Give the extent of all uninfected red blood cells.
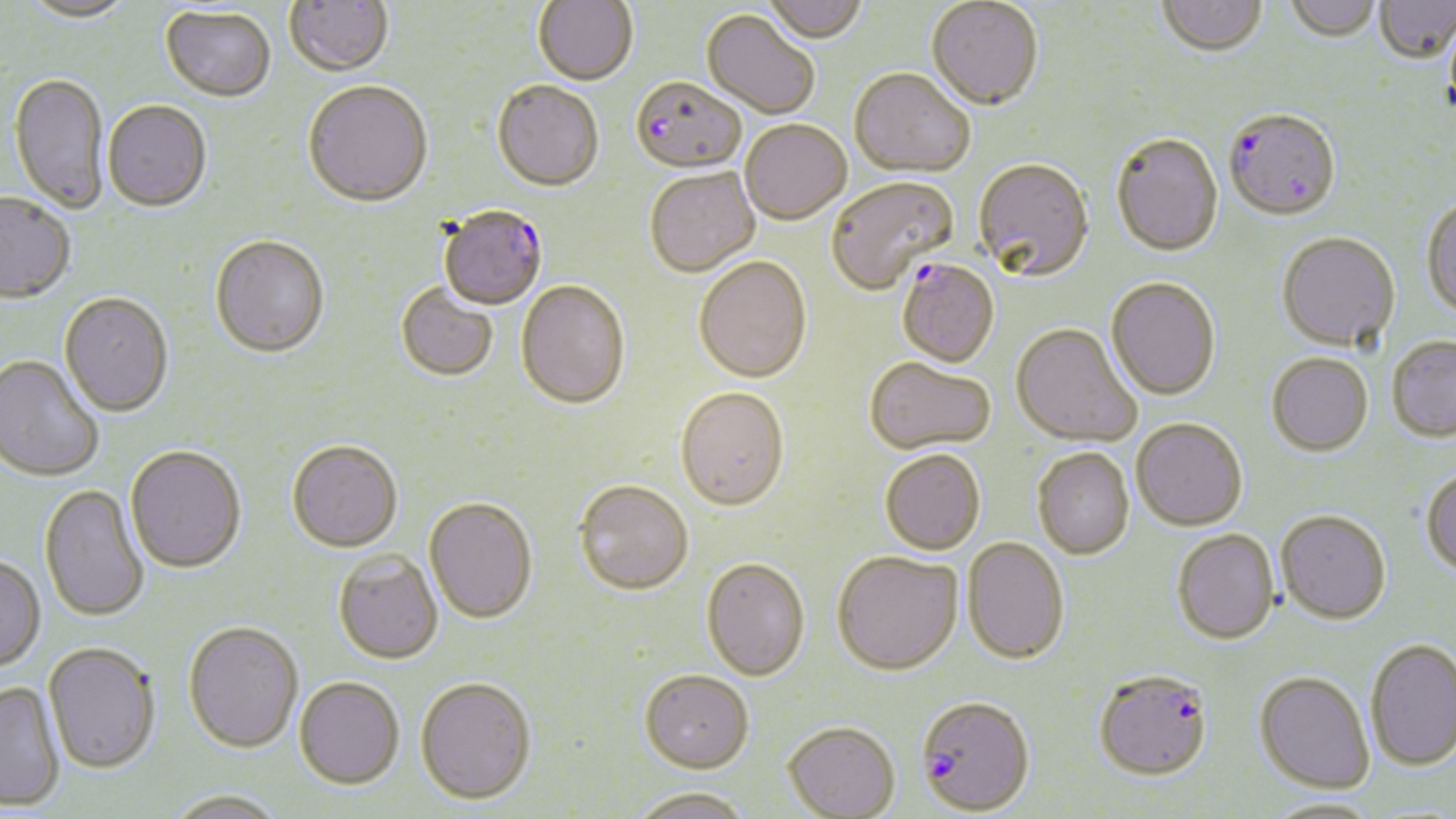

Approximate bounding boxes as (x1, y1, x2, y2) in pixels.
Uninfected red blood cells: (17, 0, 138, 24), (285, 0, 395, 78), (762, 0, 868, 45), (1284, 0, 1382, 45), (533, 1, 639, 88), (926, 1, 1044, 114), (1157, 1, 1267, 59), (1374, 1, 1456, 66), (160, 7, 276, 103), (701, 11, 819, 120), (848, 70, 975, 180), (8, 73, 109, 214), (303, 83, 432, 210), (492, 83, 604, 194), (103, 101, 212, 214), (740, 121, 852, 227), (1111, 135, 1224, 259), (973, 161, 1094, 284), (645, 169, 760, 279), (827, 178, 959, 296), (0, 194, 76, 305), (1422, 198, 1456, 323), (1277, 234, 1401, 354), (210, 238, 330, 361), (694, 258, 812, 385), (1106, 279, 1221, 401), (516, 282, 630, 413), (396, 285, 498, 383), (59, 294, 173, 419), (1011, 324, 1141, 447), (1386, 337, 1456, 443), (1266, 354, 1373, 457), (0, 356, 104, 483), (864, 359, 996, 456), (676, 389, 790, 514), (1132, 419, 1248, 532), (287, 443, 402, 555), (125, 447, 246, 575), (1032, 448, 1135, 560), (880, 450, 985, 556), (1422, 467, 1456, 580), (574, 482, 693, 597), (39, 484, 150, 622), (424, 499, 537, 626), (1275, 510, 1391, 626), (1172, 530, 1280, 646), (962, 538, 1070, 667), (334, 551, 443, 666), (833, 552, 964, 677), (0, 556, 46, 673), (701, 559, 809, 682), (183, 622, 303, 755), (1365, 638, 1456, 771), (42, 644, 160, 775), (639, 669, 754, 773), (1254, 671, 1375, 794), (414, 678, 538, 805), (294, 679, 404, 792), (0, 680, 65, 811), (783, 721, 901, 819), (627, 787, 754, 819), (164, 791, 287, 818), (1262, 796, 1384, 818).

Summary:
  - Plasmodium falciparum-infected red blood cell locations: (631, 79, 746, 176), (1224, 112, 1341, 223), (439, 208, 548, 311), (896, 261, 1000, 369), (1095, 669, 1214, 781), (916, 696, 1036, 816)
  - Slide-level diagnosis: Plasmodium falciparum
  - Stain: May-Grünwald-Giemsa
  - Field of view: one of a larger specimen
  - Modality: light microscopy
  - Preparation: thin blood film
  - Image size: 1456×819 pixels
  - Magnification: 1000x